Give the position of every malaria parasite and every leukocyte.
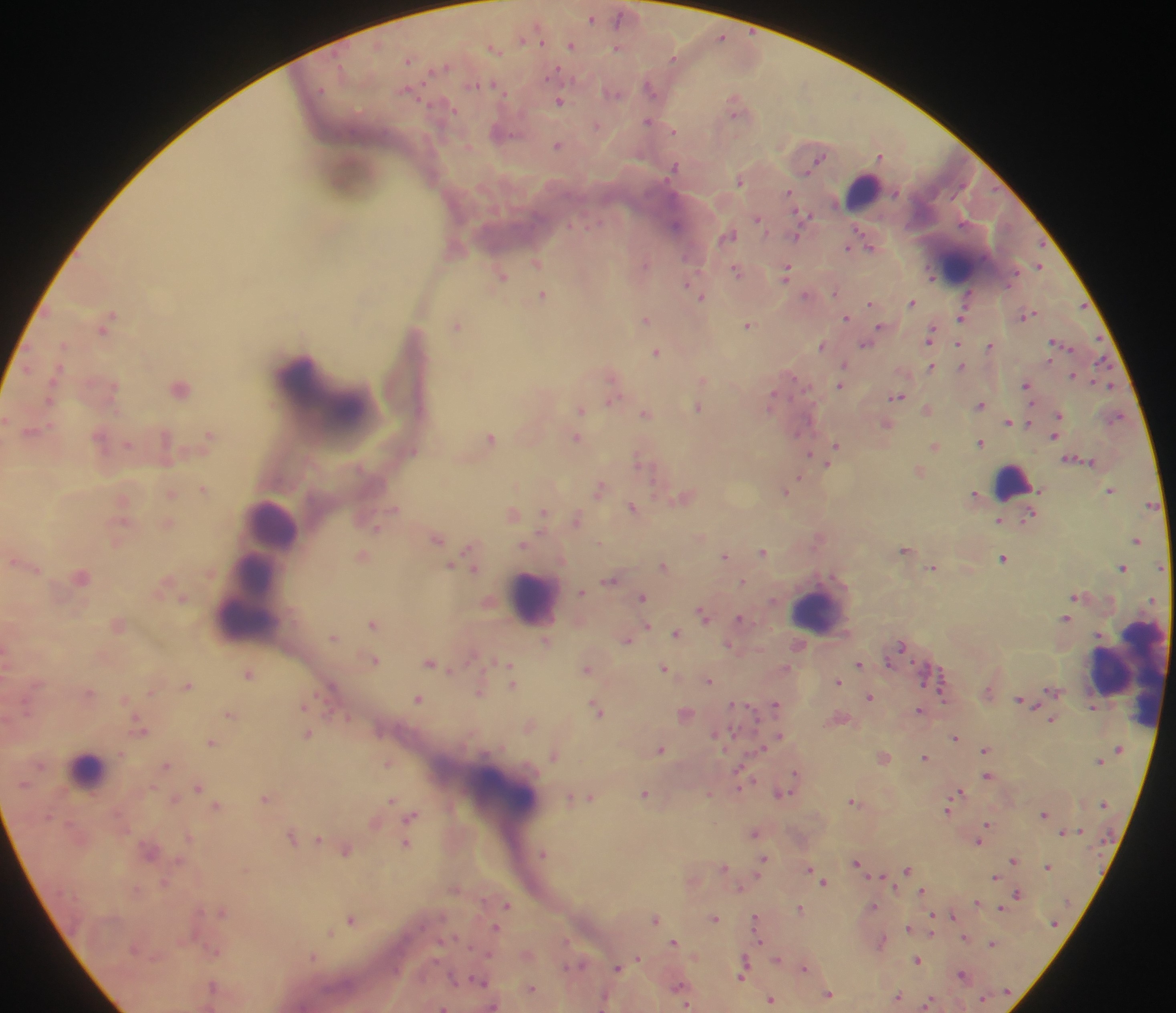
Approximate centers as {x, y} in pixels.
Malaria parasites: {591, 17}, {619, 17}, {721, 36}, {524, 38}, {571, 43}, {493, 48}, {617, 48}, {408, 58}, {673, 58}, {437, 67}, {555, 71}, {477, 83}, {649, 86}, {407, 90}, {613, 92}, {560, 101}, {734, 102}, {451, 107}, {735, 112}, {648, 121}, {596, 125}, {674, 130}, {497, 132}, {558, 145}, {881, 155}, {819, 158}, {674, 167}, {741, 180}, {788, 193}, {802, 216}, {758, 219}, {676, 225}, {334, 227}, {730, 234}, {797, 236}, {871, 245}, {849, 246}, {537, 261}, {644, 262}, {1039, 266}, {737, 270}, {787, 271}, {501, 275}, {687, 281}, {835, 290}, {542, 294}, {968, 294}, {806, 295}, {701, 297}, {870, 302}, {912, 302}, {111, 313}, {1028, 314}, {845, 316}, {962, 316}, {645, 319}, {749, 323}, {456, 325}, {879, 327}, {930, 335}, {866, 342}, {1058, 342}, {64, 344}, {821, 345}, {959, 345}, {990, 345}, {656, 351}, {1101, 363}, {844, 364}, {961, 364}, {932, 366}, {1072, 374}, {793, 377}, {702, 379}, {1027, 384}, {839, 385}, {1108, 385}, {180, 387}, {51, 396}, {897, 396}, {612, 400}, {771, 401}, {981, 405}, {698, 407}, {581, 408}, {927, 409}, {645, 413}, {1058, 414}, {1115, 417}, {1008, 421}, {888, 424}, {33, 430}, {210, 434}, {99, 436}, {1054, 436}, {491, 437}, {577, 438}, {981, 442}, {127, 445}, {837, 445}, {935, 445}, {413, 451}, {810, 453}, {639, 458}, {920, 469}, {800, 478}, {791, 483}, {599, 487}, {203, 489}, {1110, 489}, {787, 491}, {171, 493}, {974, 493}, {685, 496}, {122, 500}, {633, 506}, {394, 508}, {543, 512}, {512, 513}, {1030, 516}, {578, 518}, {999, 520}, {169, 523}, {375, 528}, {436, 538}, {1137, 539}, {523, 543}, {468, 548}, {904, 549}, {763, 551}, {725, 554}, {363, 556}, {1004, 557}, {14, 560}, {663, 564}, {451, 565}, {464, 566}, {1160, 566}, {932, 567}, {1122, 567}, {475, 568}, {82, 576}, {609, 580}, {742, 581}, {581, 591}, {1074, 596}, {642, 597}, {183, 598}, {702, 613}, {1066, 617}, {740, 618}, {372, 623}, {647, 626}, {676, 632}, {334, 636}, {626, 638}, {546, 640}, {729, 645}, {901, 645}, {375, 659}, {889, 661}, {859, 662}, {430, 663}, {513, 666}, {664, 667}, {786, 667}, {587, 668}, {248, 673}, {709, 679}, {838, 681}, {520, 682}, {188, 685}, {331, 686}, {942, 688}, {1053, 689}, {479, 691}, {89, 692}, {870, 697}, {418, 698}, {1022, 698}, {305, 703}, {735, 703}, {776, 704}, {596, 708}, {919, 709}, {229, 713}, {685, 713}, {344, 717}, {1052, 719}, {529, 725}, {139, 728}, {308, 733}, {715, 733}, {955, 736}, {778, 737}, {211, 741}, {762, 747}, {661, 748}, {985, 748}, {554, 754}, {884, 756}, {925, 757}, {388, 762}, {167, 764}, {739, 772}, {794, 775}, {987, 775}, {198, 786}, {787, 787}, {960, 790}, {781, 792}, {645, 793}, {709, 793}, {265, 797}, {571, 797}, {590, 797}, {392, 799}, {852, 800}, {217, 805}, {948, 808}, {1043, 813}, {410, 816}, {987, 823}, {1065, 831}, {754, 832}, {292, 836}, {981, 836}, {318, 838}, {977, 841}, {406, 843}, {345, 849}, {543, 853}, {763, 858}, {1013, 858}, {857, 862}, {1048, 865}, {724, 866}, {809, 869}, {908, 869}, {994, 877}, {823, 880}, {922, 891}, {1018, 893}, {977, 901}, {506, 905}, {873, 906}, {1000, 907}, {800, 908}, {222, 911}, {953, 915}, {713, 917}, {351, 918}, {655, 918}, {756, 918}, {908, 926}, {495, 927}, {330, 931}, {932, 931}, {757, 936}, {964, 937}, {566, 940}, {674, 940}, {881, 941}, {440, 942}, {992, 942}, {215, 951}, {489, 953}, {313, 955}, {638, 958}, {778, 958}, {918, 960}, {744, 962}, {578, 964}, {618, 967}, {804, 967}, {963, 973}, {742, 974}, {454, 977}, {481, 980}, {212, 985}, {677, 986}, {531, 987}, {829, 994}, {898, 996}, {771, 999}, {604, 1001}, {929, 1002}, {686, 1005}.
Leukocytes: {862, 190}, {957, 264}, {304, 374}, {350, 416}, {1011, 481}, {275, 522}, {258, 572}, {533, 597}, {816, 608}, {246, 624}, {1131, 672}, {87, 769}, {503, 792}.

country: Ghana
image_size: 1176×1013 pixels
capture: mobile-phone photograph through a microscope
preparation: thick blood smear
field_of_view: single